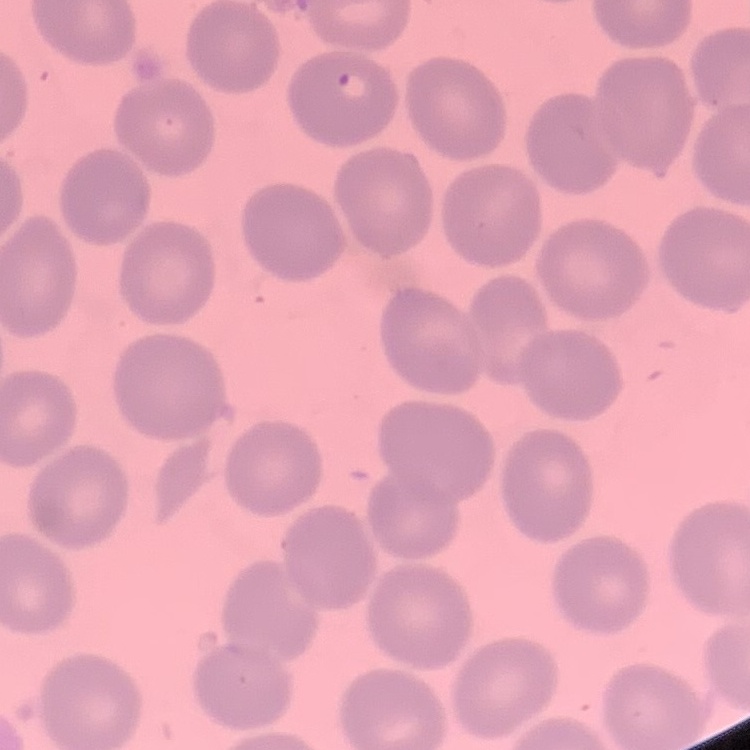

Summary:
  - Erythrocyte morphology: no rouleaux formation
  - Preparation: thin peripheral smear
  - Image type: one tile cut from a larger photomicrograph
  - Stain: Field's or Giemsa